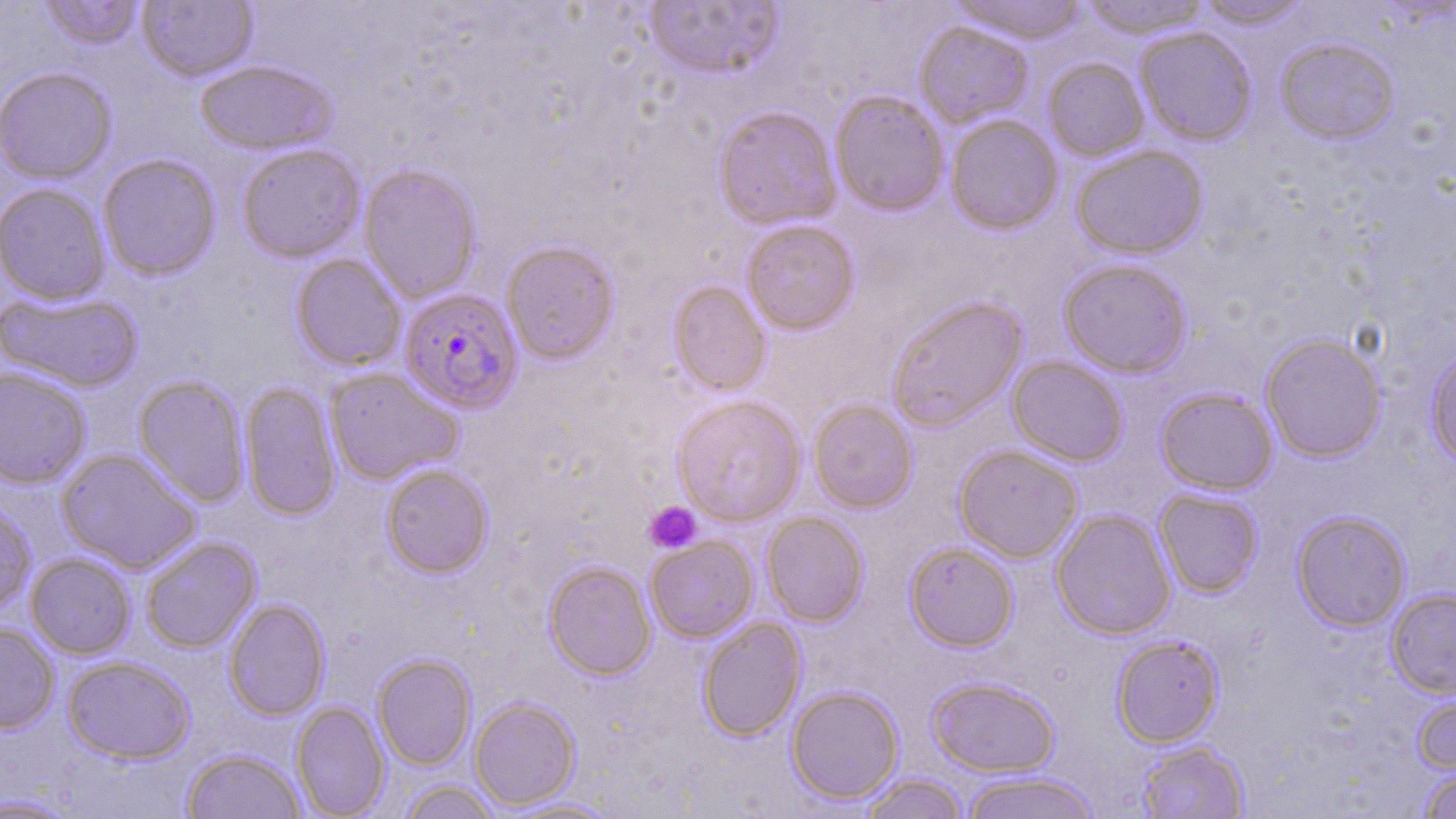

Summary:
  - Coordinate format: approximate bounding boxes as [x1, y1, x2, y2] in pixels
  - Uninfected red blood cell locations: [39, 0, 143, 51], [138, 0, 257, 82], [949, 0, 1088, 45], [1080, 0, 1213, 39], [1193, 0, 1313, 29], [643, 1, 783, 80], [915, 21, 1034, 128], [1135, 27, 1257, 146], [1275, 37, 1401, 145], [1043, 58, 1149, 162], [195, 60, 336, 155], [1, 68, 117, 184], [830, 91, 949, 217], [712, 106, 841, 230], [945, 115, 1063, 235], [237, 144, 366, 262], [1070, 145, 1208, 260], [98, 154, 221, 280], [359, 163, 482, 303], [0, 184, 111, 305], [741, 220, 860, 335], [501, 240, 620, 365], [290, 253, 406, 372], [1058, 258, 1192, 378], [668, 281, 771, 396], [1, 290, 142, 393], [886, 295, 1027, 433], [1260, 333, 1387, 462], [1425, 346, 1456, 469], [1007, 356, 1129, 467], [0, 367, 92, 489], [325, 367, 463, 485], [133, 376, 249, 507], [239, 381, 342, 521], [1155, 388, 1278, 495], [671, 395, 806, 526], [808, 399, 919, 513], [954, 445, 1083, 563], [56, 449, 201, 574], [380, 463, 494, 578], [1154, 489, 1264, 597], [0, 501, 36, 617], [1051, 509, 1176, 639], [1291, 510, 1412, 632], [761, 512, 869, 626], [645, 536, 758, 643], [141, 537, 261, 653], [904, 542, 1018, 651], [26, 553, 135, 659], [543, 561, 656, 680], [1387, 588, 1456, 698], [224, 598, 330, 720], [697, 617, 807, 741], [0, 622, 59, 734], [1111, 635, 1224, 748], [372, 653, 477, 771], [61, 656, 194, 764], [926, 676, 1060, 777], [786, 685, 904, 805], [1412, 689, 1456, 776], [469, 697, 581, 811], [291, 701, 390, 818], [1137, 741, 1250, 818], [182, 748, 305, 819], [1419, 769, 1456, 819], [959, 771, 1103, 819], [859, 773, 969, 819], [397, 780, 502, 819], [0, 793, 81, 817], [496, 796, 623, 818]
  - Plasmodium falciparum-infected red blood cell locations: [398, 288, 523, 414]
  - Platelet locations: [644, 501, 702, 554]
  - Slide-level diagnosis: Plasmodium falciparum
  - Preparation: thin blood film
  - Field of view: one of a larger specimen
  - Image size: 1456×819 pixels
  - Magnification: 1000x
  - Stain: May-Grünwald-Giemsa
  - Modality: light microscopy